Give the preparation type.
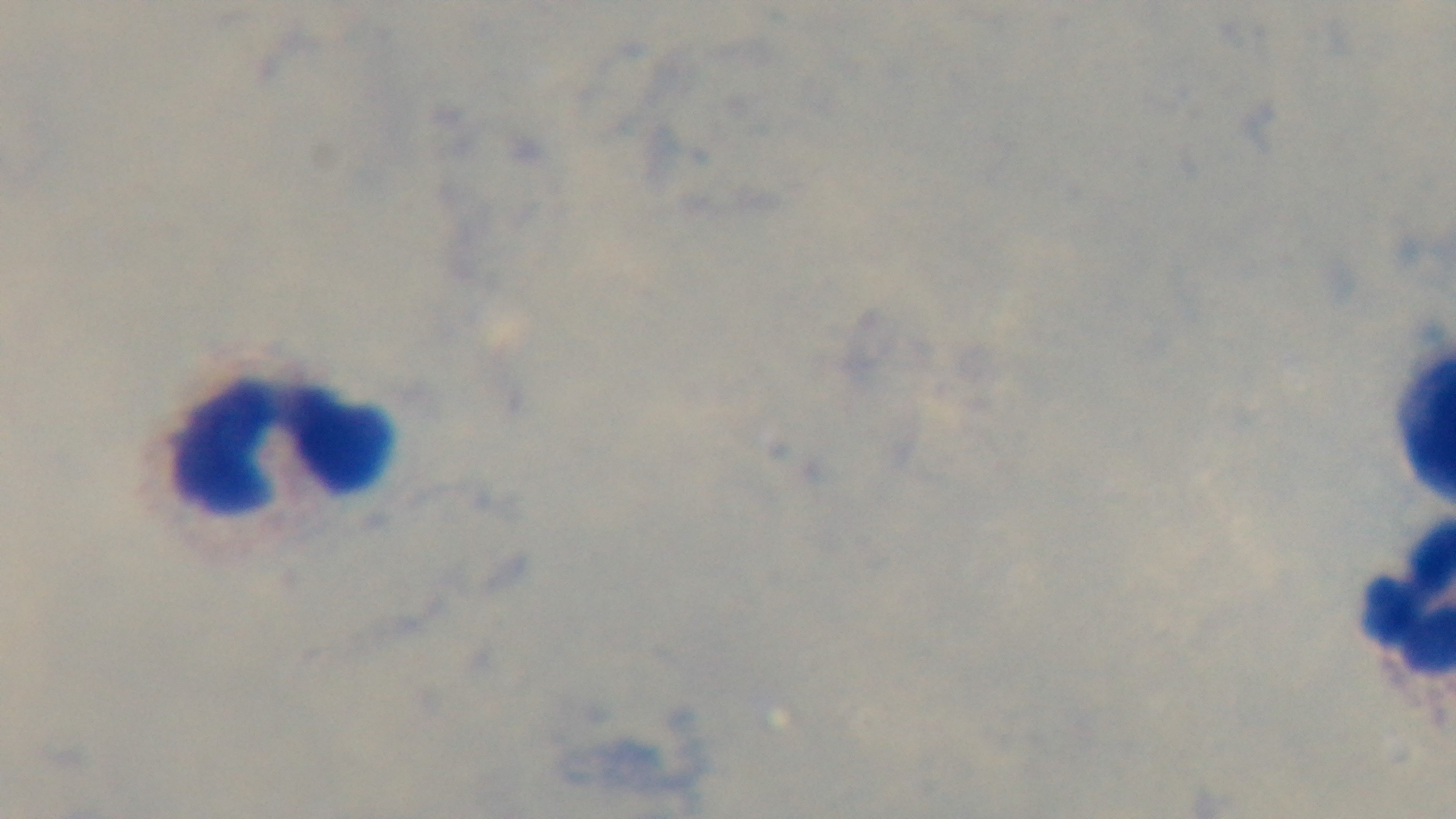
It is a thick blood film.

Giemsa stain. 100x oil-immersion objective. Mounted 4K digital camera. One field from the slide. Photomicrograph. Malaria status: uninfected.